Name the parasite shown.
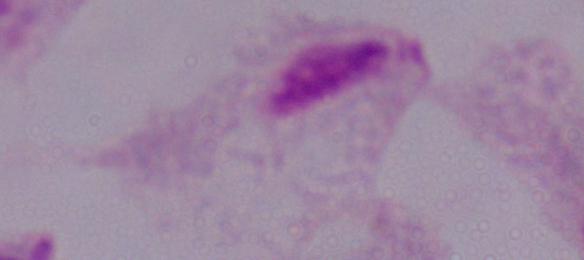
This is a trichomonad.

1000x magnification. Micrograph.